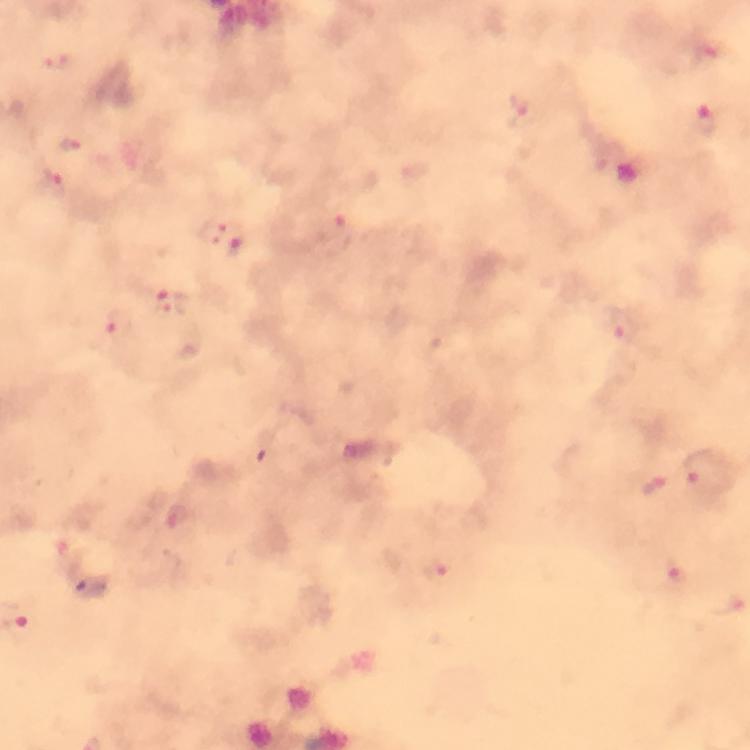

Approximate centers as [x, y] in pixels.
Summary:
  - Malaria parasite locations: [60, 61], [519, 110], [707, 123], [71, 145], [56, 182], [211, 230], [333, 230], [235, 247], [171, 303], [121, 326], [622, 327], [699, 467], [654, 487], [673, 571], [438, 572]
  - Preparation: thick smear
  - Image size: 750×750 pixels
  - Stain: Giemsa
  - Immersion oil: used
  - Magnification: 100x
  - Context: from a malaria diagnostic workup
  - Cropped from: one field of view
  - Capture: smartphone photograph through a microscope